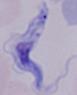

Micrograph. 1000x magnification. A trypanosome is seen.